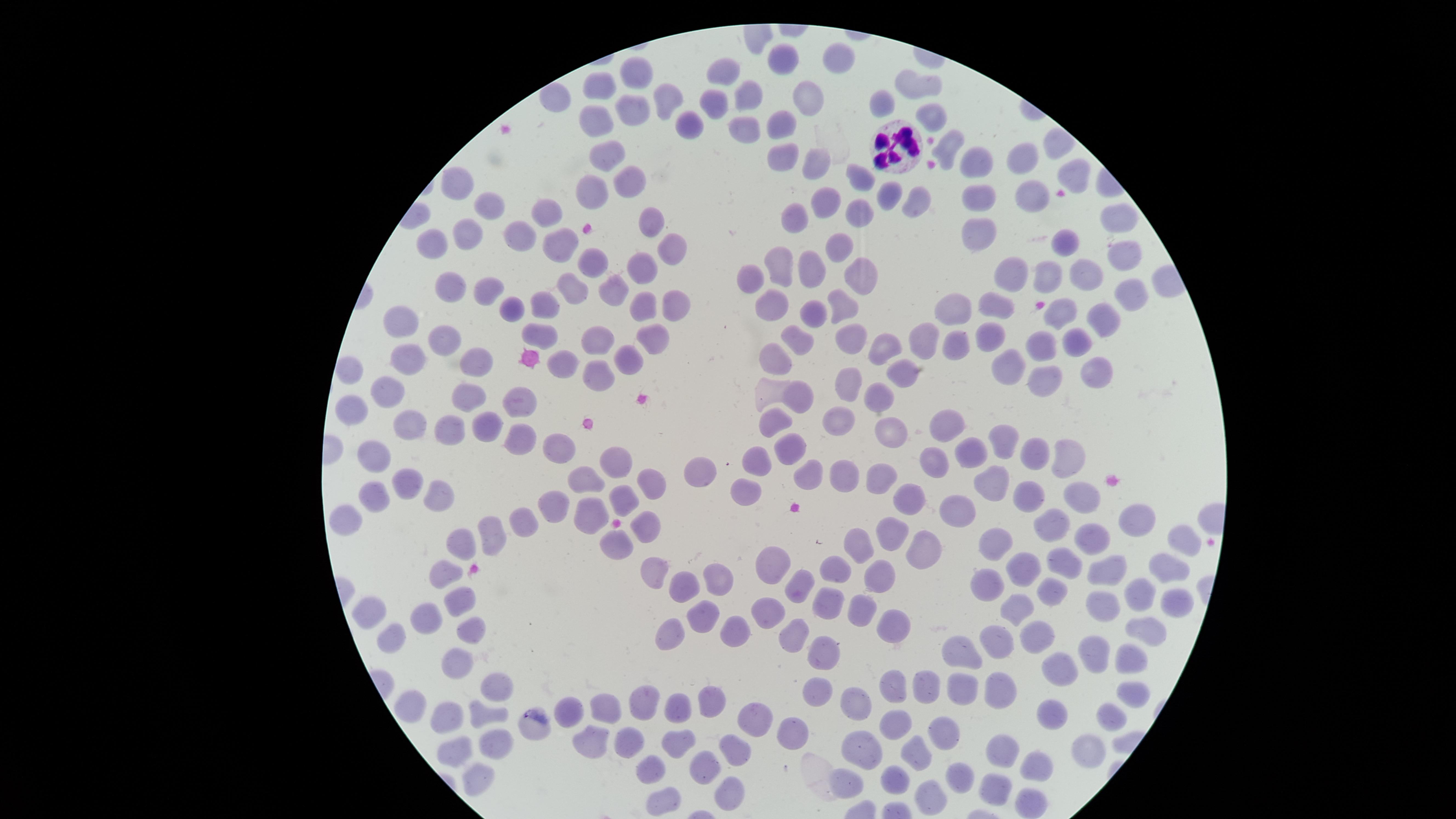
Approximate marker points, in pixels from the top-left corner.
Summary:
  - Uninfected RBCs: (x=790, y=65), (x=834, y=65), (x=727, y=70), (x=636, y=78), (x=916, y=86), (x=601, y=91), (x=670, y=96), (x=555, y=97), (x=752, y=97), (x=811, y=99), (x=716, y=100), (x=633, y=103), (x=881, y=104), (x=931, y=115), (x=595, y=117), (x=779, y=124), (x=688, y=125), (x=744, y=132), (x=948, y=146), (x=611, y=153), (x=1020, y=154), (x=780, y=155), (x=975, y=163), (x=818, y=165), (x=1071, y=174), (x=628, y=175), (x=861, y=183), (x=456, y=184), (x=590, y=187), (x=1027, y=190), (x=981, y=196), (x=482, y=202), (x=889, y=202), (x=831, y=205), (x=918, y=205), (x=548, y=207), (x=861, y=211), (x=1115, y=215), (x=649, y=219), (x=799, y=219), (x=466, y=231), (x=982, y=234), (x=522, y=235), (x=1069, y=244), (x=566, y=245), (x=437, y=246), (x=674, y=246), (x=839, y=247), (x=1122, y=250), (x=592, y=264), (x=782, y=267), (x=645, y=271), (x=816, y=271), (x=1012, y=271), (x=858, y=273), (x=1085, y=273), (x=1049, y=277), (x=751, y=281), (x=577, y=283), (x=456, y=288), (x=612, y=289), (x=489, y=290), (x=1131, y=292), (x=776, y=301), (x=843, y=303), (x=677, y=304), (x=543, y=305), (x=998, y=305), (x=510, y=309), (x=642, y=309), (x=959, y=309), (x=1060, y=313), (x=815, y=316), (x=1102, y=320), (x=404, y=324), (x=536, y=330), (x=994, y=333), (x=852, y=336), (x=598, y=337), (x=654, y=337), (x=924, y=337), (x=1040, y=338), (x=1075, y=340), (x=444, y=341), (x=801, y=341), (x=956, y=342), (x=884, y=346), (x=775, y=349), (x=632, y=356), (x=413, y=361), (x=566, y=362), (x=474, y=363), (x=350, y=365), (x=1010, y=366), (x=1096, y=366), (x=603, y=371), (x=906, y=372), (x=1041, y=381), (x=847, y=388), (x=390, y=390), (x=801, y=395), (x=466, y=399), (x=522, y=399), (x=876, y=399), (x=347, y=413), (x=837, y=419), (x=773, y=423), (x=411, y=425), (x=485, y=425), (x=943, y=426), (x=453, y=427), (x=889, y=429), (x=519, y=439), (x=998, y=441), (x=562, y=448), (x=794, y=448), (x=1068, y=448), (x=967, y=451), (x=1035, y=451), (x=761, y=457), (x=378, y=459), (x=622, y=461), (x=940, y=461), (x=699, y=472), (x=811, y=478), (x=842, y=479), (x=992, y=480), (x=582, y=481), (x=408, y=482), (x=878, y=484), (x=653, y=485), (x=1082, y=490), (x=747, y=491), (x=1031, y=493), (x=380, y=494), (x=440, y=494), (x=908, y=496), (x=624, y=498), (x=959, y=506), (x=556, y=507), (x=593, y=510), (x=528, y=520), (x=1132, y=520), (x=350, y=521), (x=1059, y=523), (x=648, y=525), (x=499, y=532), (x=896, y=532), (x=1094, y=534), (x=461, y=542), (x=616, y=543), (x=864, y=544), (x=999, y=544), (x=1183, y=545), (x=927, y=552), (x=774, y=561), (x=1068, y=563), (x=1165, y=565), (x=657, y=567), (x=1026, y=567), (x=839, y=570), (x=1107, y=571), (x=447, y=572), (x=882, y=574), (x=713, y=579), (x=992, y=579), (x=794, y=586), (x=680, y=590), (x=1051, y=593), (x=1142, y=596), (x=460, y=598), (x=831, y=603), (x=1018, y=603), (x=1107, y=603), (x=1176, y=603), (x=861, y=607), (x=373, y=611), (x=773, y=613), (x=431, y=617), (x=703, y=618), (x=890, y=621), (x=1149, y=623), (x=473, y=624), (x=737, y=632), (x=671, y=633), (x=1037, y=635), (x=794, y=636), (x=393, y=637), (x=995, y=641), (x=1100, y=645), (x=824, y=650), (x=963, y=651), (x=459, y=657), (x=1125, y=657), (x=1062, y=664), (x=498, y=679), (x=892, y=684), (x=961, y=685), (x=819, y=687), (x=998, y=687), (x=921, y=688), (x=1131, y=694), (x=855, y=698), (x=714, y=701), (x=645, y=702), (x=400, y=703), (x=681, y=707), (x=443, y=711), (x=609, y=711), (x=570, y=712), (x=486, y=713), (x=1115, y=715), (x=1054, y=716), (x=901, y=720), (x=757, y=721), (x=945, y=728), (x=794, y=729), (x=535, y=730), (x=498, y=740), (x=628, y=740), (x=594, y=741), (x=678, y=741), (x=458, y=749), (x=1090, y=750), (x=860, y=751), (x=728, y=753), (x=1001, y=753), (x=915, y=757), (x=657, y=763), (x=707, y=766), (x=1039, y=767), (x=478, y=772), (x=893, y=776), (x=960, y=776), (x=850, y=784), (x=999, y=785), (x=724, y=792), (x=934, y=795), (x=669, y=798), (x=1029, y=802)
  - WBCs: (x=904, y=142)
  - Capture: smartphone photograph through the microscope eyepiece
  - Field of view: single
  - Presence: no malaria parasites detected
  - Image size: 1456×819 pixels
  - Preparation: thin smear of blood
  - Visible region: circular
  - Stain: Giemsa